Describe the morphology of the red blood cells.
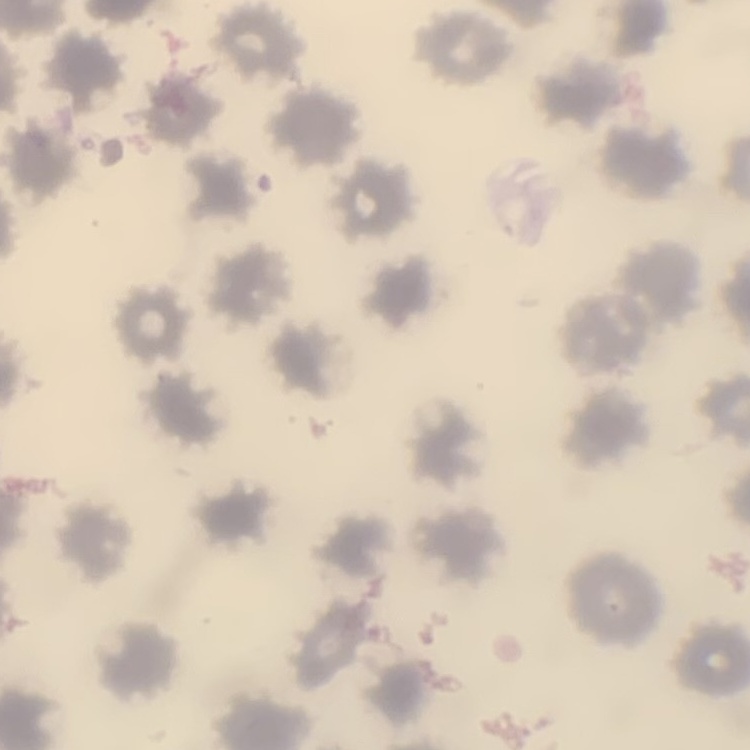

No rouleaux formation.

image_type: one tile cut from a larger photomicrograph
stain: Field's or Giemsa
preparation: thin blood smear